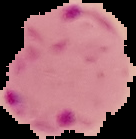
Summary:
  - Preparation: thin blood film
  - Image type: cell region segmented out of the field of view; surrounding area masked to black
  - Malaria status: parasitized
  - Image size: 136×139 pixels